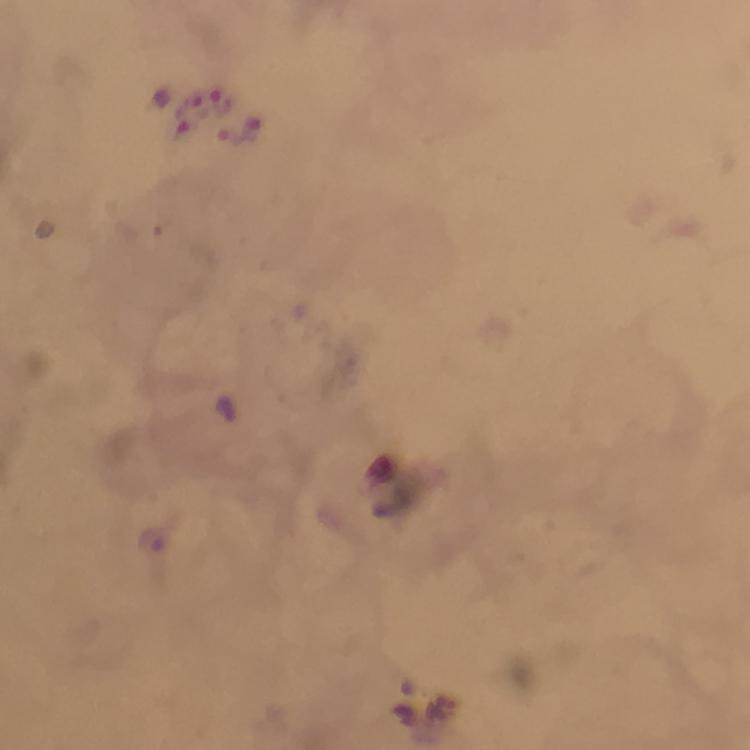
Plasmodium parasite locations = approximate centers as [x, y] in pixels: [222, 102], [227, 411], [152, 541]
image size = 750×750 pixels
immersion oil = used
preparation = thick blood film
stain = Giemsa
cropped from = one field of view
capture = smartphone mounted on the microscope
magnification = 100x
context = from a diagnostic examination for malaria